Assess the morphology of the red blood cells.
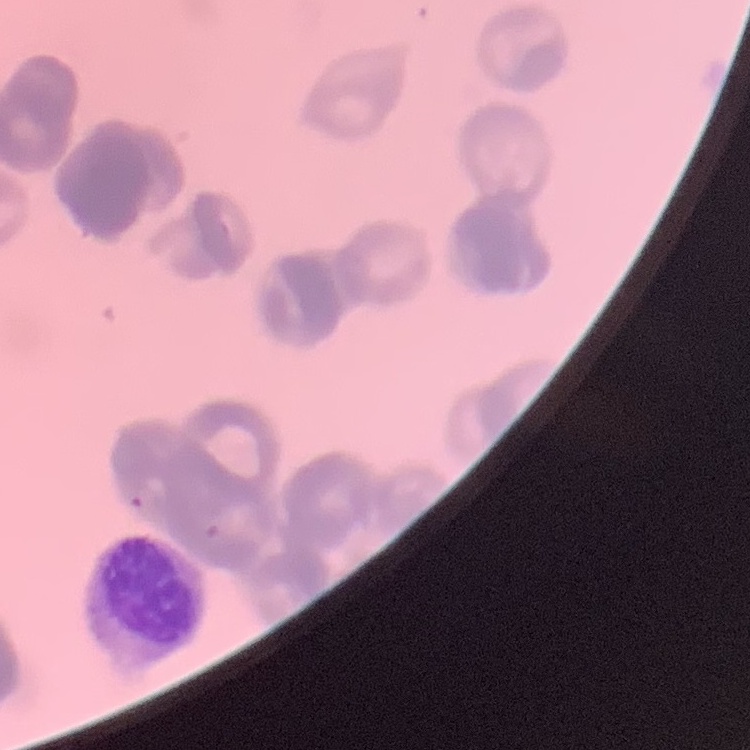

They show rouleaux formation.

preparation = thin peripheral smear
stain = Field's or Giemsa
image type = one tile cut from a larger photomicrograph